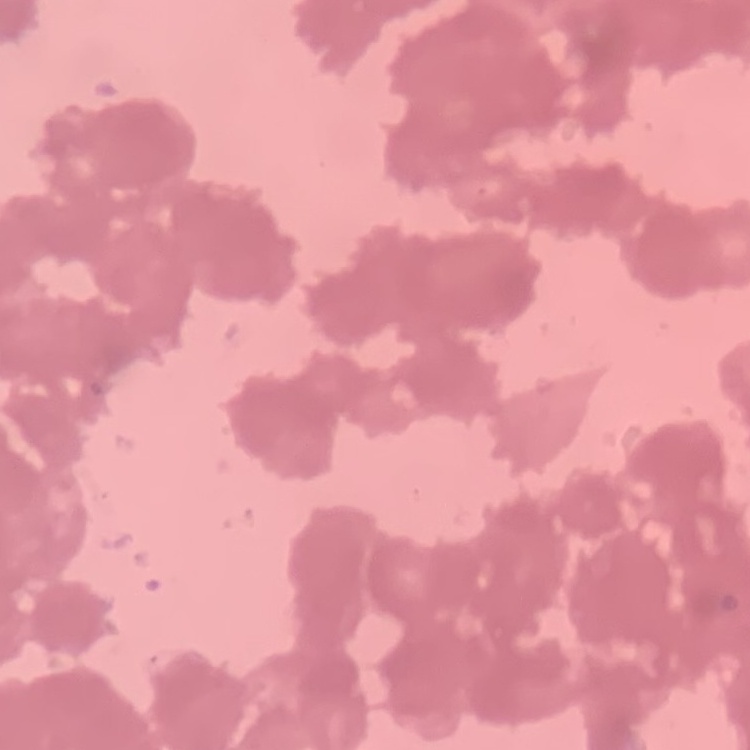
red blood cell morphology = rouleaux formation
preparation = thin blood film
stain = Field's or Giemsa
image type = one tile cut from a larger photomicrograph